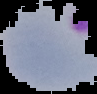
Summary:
  - Image type: segmented cell region on a black background
  - Result: Plasmodium parasites detected
  - Image size: 97×94 pixels
  - Preparation: thin blood smear